Classify this cell by malaria status.
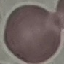
Uninfected.

preparation = thin blood smear
image type = cell patch, automatically extracted from a larger field of view and resized to 64 × 64 pixels
stain = Giemsa
capture = smartphone through the microscope eyepiece